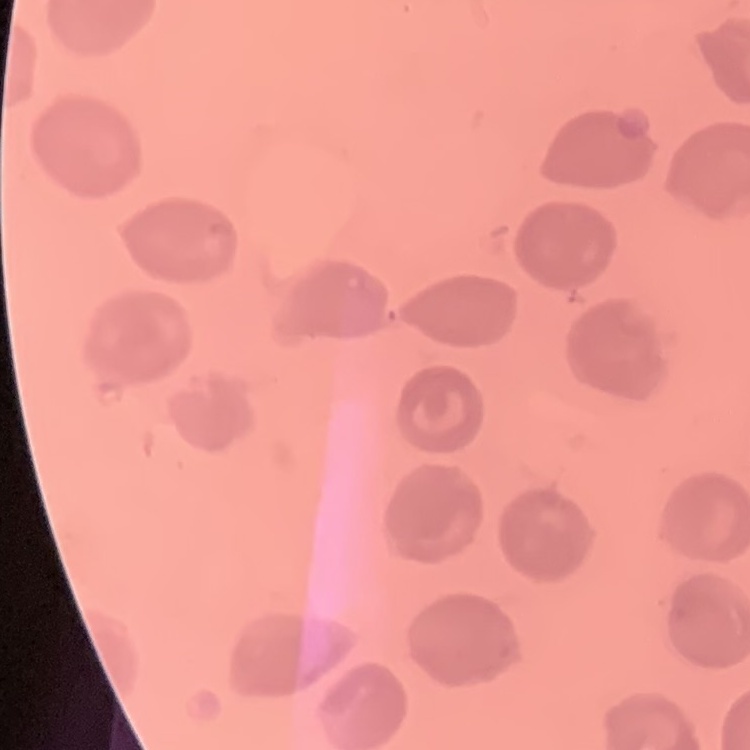 The erythrocytes show no rouleaux formation. Thin blood smear. Square crop of a larger photomicrograph. Field's or Giemsa stain.